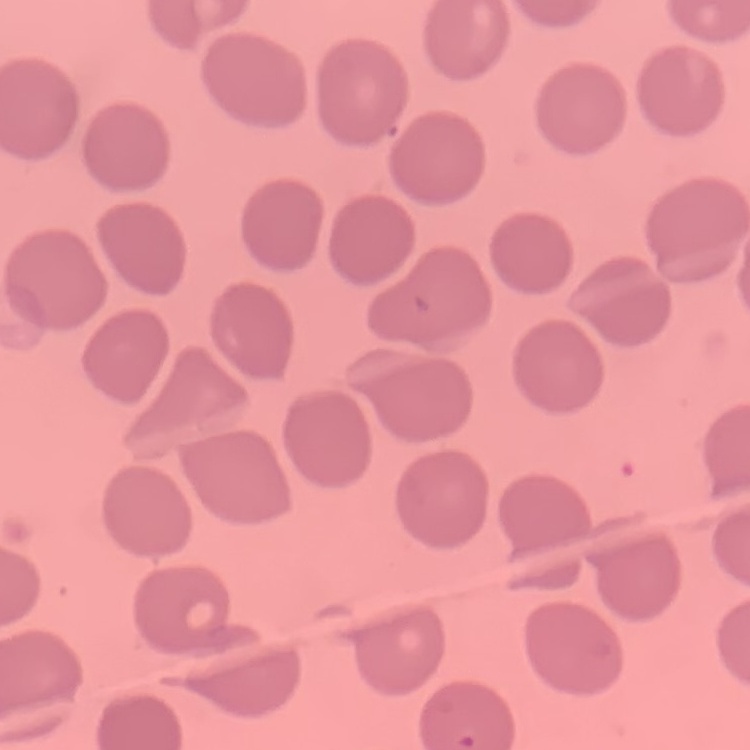

Summary:
  - Red blood cell morphology: no rouleaux formation
  - Preparation: thin blood film
  - Stain: Field's or Giemsa
  - Image type: one tile cut from a larger photomicrograph